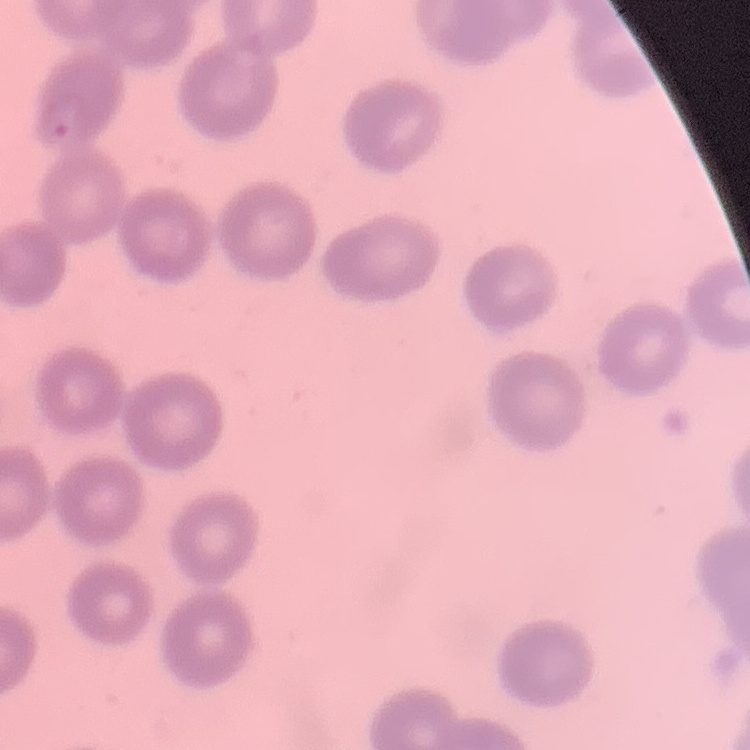
Summary:
  - Erythrocyte morphology: no rouleaux formation
  - Stain: Field's or Giemsa
  - Preparation: thin blood smear
  - Image type: one tile cut from a larger photomicrograph